Comment on the morphology of the red blood cells.
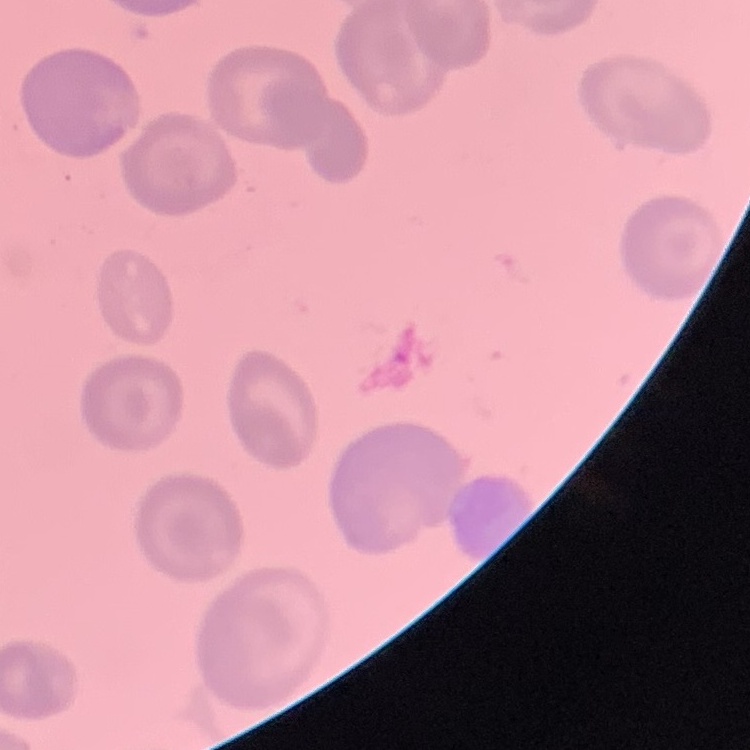
No rouleaux formation.

preparation: thin blood film
image_type: square crop of a larger photomicrograph
stain: Field's or Giemsa